Identify the parasite.
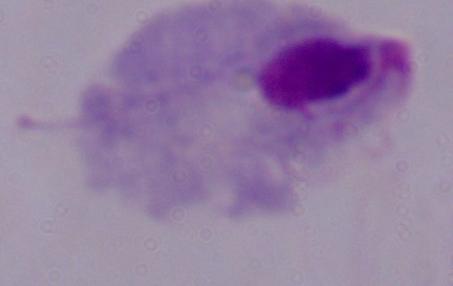
A trichomonad.

Photomicrograph. Captured at 1000x magnification.